Locate every malaria parasite and every leukocyte.
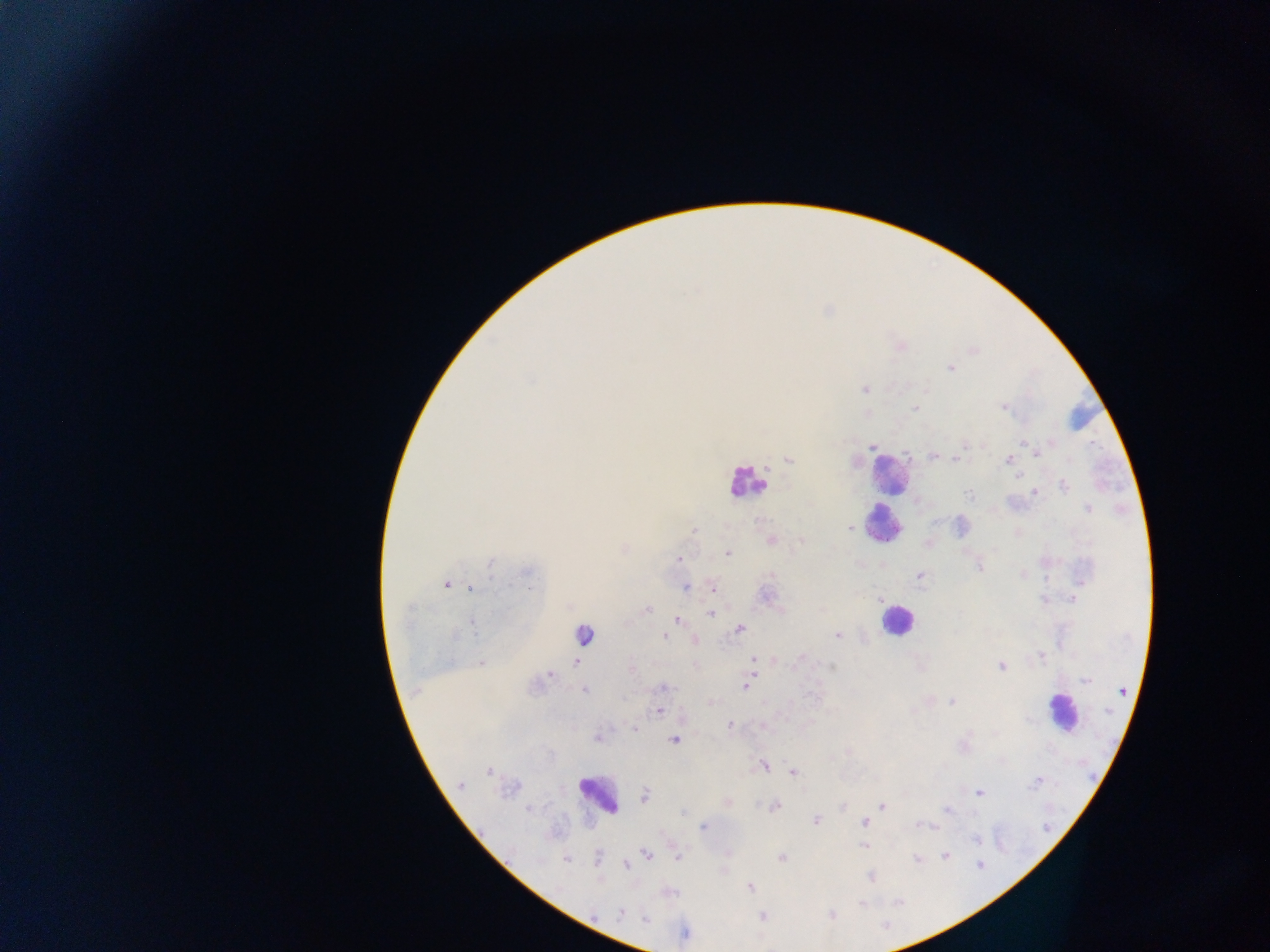
Approximate centers as (x, y) in pixels.
Malaria parasites: (950, 368), (532, 381), (865, 389), (915, 408), (1003, 408), (1052, 442), (1023, 443), (964, 445), (872, 447), (1036, 451), (933, 456), (958, 459), (789, 460), (1009, 460), (1017, 476), (1064, 486), (1034, 493), (969, 495), (1087, 509), (935, 522), (851, 529), (852, 529), (694, 530), (771, 540), (802, 541), (727, 553), (679, 559), (491, 563), (980, 567), (527, 573), (772, 575), (919, 576), (446, 585), (685, 587), (470, 588), (714, 589), (766, 595), (1073, 599), (878, 600), (1044, 601), (646, 610), (710, 613), (677, 619), (473, 626), (740, 628), (455, 635), (838, 635), (665, 636), (695, 641), (1041, 656), (753, 659), (575, 663), (798, 663), (482, 664), (831, 667), (1001, 667), (631, 668), (550, 674), (1085, 681), (745, 687), (664, 688), (584, 690), (1121, 691), (952, 701), (659, 711), (1108, 711), (729, 725), (634, 728), (597, 736), (673, 740), (764, 765), (488, 771), (793, 772), (1037, 781), (460, 785), (979, 793), (645, 796), (727, 801), (881, 806), (775, 808), (527, 809), (947, 809), (683, 812), (815, 820), (864, 822), (917, 824), (925, 825), (703, 826), (976, 840), (863, 846), (646, 854), (678, 856), (946, 856), (781, 857), (599, 858), (916, 858), (566, 859), (626, 865), (980, 865), (870, 876), (750, 887), (862, 903), (620, 913), (831, 915), (763, 916), (646, 919), (686, 934).
Leukocytes: (890, 473), (745, 482), (885, 524), (896, 621), (588, 634), (1061, 712), (598, 794).

Summary:
  - Capture: mobile-phone photograph through a microscope
  - Country: Ghana
  - Image size: 1270×952 pixels
  - Field of view: single
  - Preparation: thick blood film